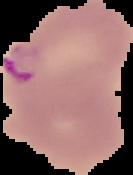

Segmented cell region on a black background. From a thin blood smear. Image is 133×175 pixels. Malaria status: parasitized.